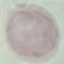
{
  "malaria_status": "uninfected",
  "stain": "Giemsa",
  "image_type": "automatically extracted cell patch, resized to 64 × 64 pixels",
  "preparation": "thin smear",
  "capture": "smartphone through the microscope eyepiece"
}